Give the extent of all Babesia divergens-infected red blood cells.
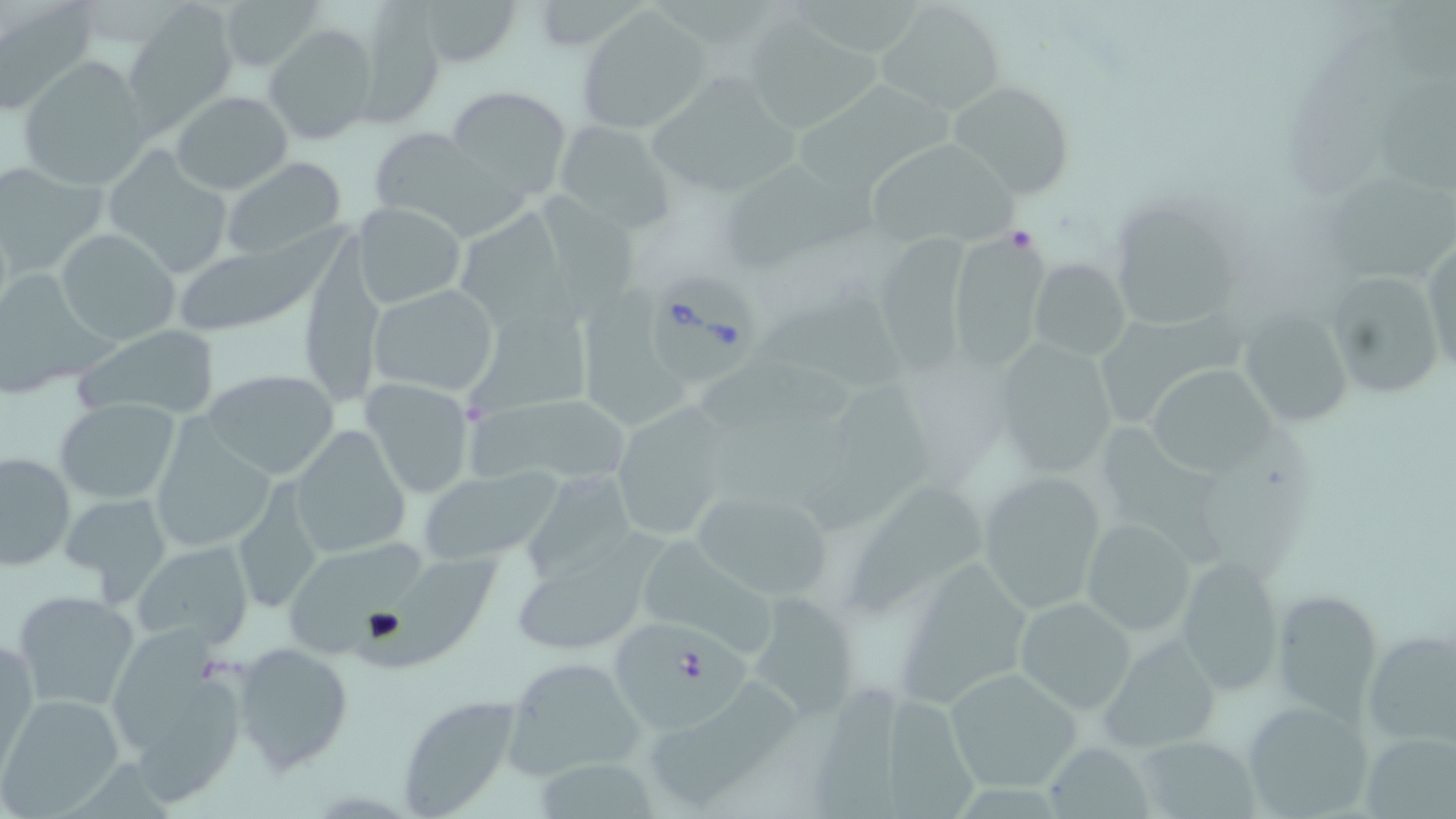

Approximate bounding boxes as named x1/y1/x2/y2 corners in pixels.
Babesia divergens-infected red blood cells: (x1=650, y1=274, x2=763, y2=386), (x1=610, y1=616, x2=751, y2=741).

Uninfected red blood cell locations: (x1=218, y1=0, x2=328, y2=74), (x1=412, y1=0, x2=525, y2=68), (x1=1387, y1=0, x2=1456, y2=94), (x1=546, y1=2, x2=652, y2=53), (x1=874, y1=2, x2=1005, y2=114), (x1=122, y1=4, x2=240, y2=130), (x1=349, y1=4, x2=446, y2=126), (x1=0, y1=5, x2=96, y2=116), (x1=576, y1=6, x2=707, y2=133), (x1=743, y1=15, x2=896, y2=132), (x1=264, y1=23, x2=379, y2=147), (x1=17, y1=56, x2=152, y2=188), (x1=652, y1=70, x2=809, y2=195), (x1=945, y1=80, x2=1075, y2=201), (x1=798, y1=82, x2=963, y2=188), (x1=1386, y1=82, x2=1456, y2=195), (x1=445, y1=85, x2=573, y2=199), (x1=170, y1=90, x2=292, y2=193), (x1=118, y1=108, x2=285, y2=239), (x1=553, y1=122, x2=675, y2=231), (x1=365, y1=126, x2=510, y2=235), (x1=865, y1=136, x2=1021, y2=247), (x1=105, y1=148, x2=234, y2=277), (x1=223, y1=157, x2=347, y2=258), (x1=719, y1=157, x2=894, y2=275), (x1=0, y1=161, x2=108, y2=278), (x1=1327, y1=167, x2=1456, y2=276), (x1=536, y1=187, x2=642, y2=331), (x1=1111, y1=198, x2=1237, y2=335), (x1=354, y1=202, x2=466, y2=308), (x1=466, y1=210, x2=568, y2=331), (x1=182, y1=218, x2=354, y2=332), (x1=55, y1=229, x2=180, y2=346), (x1=1422, y1=240, x2=1455, y2=381), (x1=945, y1=245, x2=1064, y2=374), (x1=1029, y1=257, x2=1130, y2=362), (x1=0, y1=267, x2=113, y2=397), (x1=1324, y1=268, x2=1447, y2=400), (x1=576, y1=280, x2=701, y2=429), (x1=368, y1=285, x2=501, y2=396), (x1=760, y1=287, x2=915, y2=400), (x1=460, y1=294, x2=606, y2=421), (x1=1240, y1=310, x2=1355, y2=427), (x1=73, y1=326, x2=223, y2=419), (x1=989, y1=335, x2=1121, y2=483), (x1=1145, y1=354, x2=1289, y2=480), (x1=699, y1=362, x2=859, y2=428), (x1=202, y1=368, x2=340, y2=480), (x1=359, y1=379, x2=476, y2=496), (x1=810, y1=381, x2=936, y2=534), (x1=236, y1=385, x2=377, y2=531), (x1=55, y1=398, x2=181, y2=504), (x1=463, y1=399, x2=636, y2=486), (x1=612, y1=404, x2=733, y2=540), (x1=713, y1=413, x2=862, y2=505), (x1=1102, y1=421, x2=1231, y2=571), (x1=149, y1=425, x2=275, y2=554), (x1=291, y1=426, x2=412, y2=561), (x1=0, y1=450, x2=76, y2=571), (x1=523, y1=468, x2=635, y2=587), (x1=975, y1=468, x2=1111, y2=616), (x1=418, y1=469, x2=561, y2=565), (x1=231, y1=480, x2=325, y2=615), (x1=850, y1=480, x2=988, y2=611), (x1=688, y1=486, x2=837, y2=601), (x1=59, y1=490, x2=173, y2=600), (x1=1079, y1=519, x2=1197, y2=636), (x1=643, y1=536, x2=772, y2=653), (x1=132, y1=541, x2=255, y2=650), (x1=290, y1=543, x2=428, y2=660), (x1=508, y1=547, x2=650, y2=657), (x1=355, y1=548, x2=503, y2=680), (x1=1175, y1=555, x2=1286, y2=695), (x1=897, y1=564, x2=1039, y2=707), (x1=11, y1=589, x2=142, y2=714), (x1=1273, y1=590, x2=1382, y2=714), (x1=754, y1=591, x2=866, y2=720), (x1=1016, y1=596, x2=1138, y2=713), (x1=1362, y1=627, x2=1456, y2=749), (x1=109, y1=630, x2=220, y2=753), (x1=1100, y1=634, x2=1220, y2=753), (x1=1, y1=638, x2=39, y2=777), (x1=229, y1=641, x2=353, y2=775), (x1=501, y1=656, x2=642, y2=778), (x1=945, y1=668, x2=1083, y2=792), (x1=136, y1=679, x2=251, y2=808), (x1=812, y1=687, x2=901, y2=819), (x1=650, y1=690, x2=806, y2=804), (x1=883, y1=691, x2=979, y2=819), (x1=0, y1=694, x2=123, y2=813), (x1=395, y1=694, x2=523, y2=816), (x1=1240, y1=700, x2=1375, y2=818), (x1=1361, y1=729, x2=1455, y2=819), (x1=1135, y1=733, x2=1260, y2=818), (x1=1042, y1=743, x2=1157, y2=818), (x1=541, y1=756, x2=667, y2=819). Slide-level diagnosis: Babesia divergens. Image is 1456×819 pixels. Light microscopy. One field of a larger specimen. May-Grünwald-Giemsa-stained preparation. Thin blood smear. Captured at 1000x magnification.